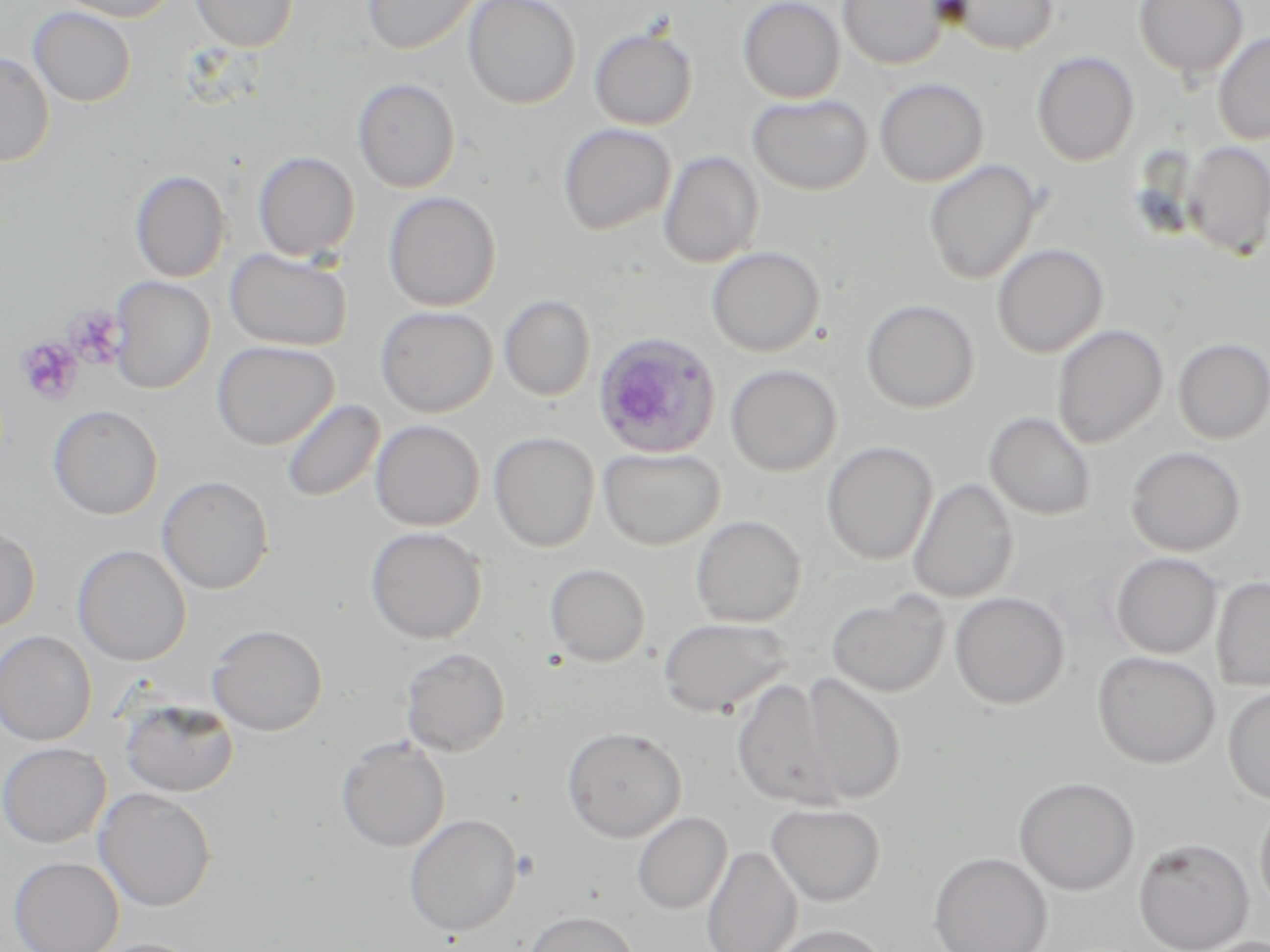

Approximate bounding boxes as [x1, y1, x2, y2] in pixels. Uninfected red blood cell locations: [52, 0, 182, 22], [190, 0, 298, 50], [362, 0, 483, 55], [463, 0, 581, 109], [737, 0, 846, 103], [837, 0, 950, 69], [944, 0, 1059, 56], [1133, 0, 1249, 80], [28, 6, 137, 107], [589, 26, 698, 130], [1213, 32, 1270, 145], [0, 51, 55, 167], [1032, 51, 1139, 166], [352, 78, 460, 193], [874, 78, 989, 187], [746, 93, 874, 196], [557, 123, 676, 235], [1183, 141, 1270, 258], [252, 150, 360, 262], [658, 151, 763, 268], [923, 159, 1044, 286], [130, 169, 230, 283], [382, 191, 502, 311], [992, 243, 1108, 358], [706, 246, 824, 357], [225, 247, 352, 351], [108, 275, 215, 394], [499, 294, 596, 401], [860, 299, 980, 413], [375, 305, 497, 417], [1051, 323, 1169, 448], [1172, 337, 1270, 444], [211, 340, 339, 450], [725, 364, 842, 477], [280, 398, 386, 503], [47, 403, 164, 520], [984, 411, 1096, 521], [370, 419, 485, 531], [489, 431, 599, 552], [821, 441, 938, 566], [597, 446, 725, 550], [1124, 446, 1246, 556], [157, 475, 274, 595], [907, 478, 1019, 604], [690, 514, 807, 627], [0, 526, 41, 632], [364, 526, 488, 644], [72, 544, 191, 666], [1110, 552, 1222, 659], [544, 563, 651, 667], [1211, 576, 1270, 691], [826, 591, 950, 697], [949, 591, 1070, 710], [658, 617, 793, 718], [207, 624, 327, 736], [0, 630, 97, 745], [399, 647, 511, 756], [1092, 651, 1221, 768], [797, 671, 906, 805], [730, 676, 844, 810], [1223, 685, 1270, 804], [119, 695, 239, 797], [562, 725, 686, 842], [335, 736, 451, 853], [0, 742, 110, 848], [1013, 776, 1140, 896], [93, 787, 217, 912], [1254, 797, 1270, 917], [766, 802, 887, 907], [631, 811, 732, 915], [404, 813, 522, 937], [1133, 837, 1255, 952], [700, 845, 802, 952], [927, 851, 1053, 952], [8, 855, 124, 952], [522, 910, 641, 952], [769, 923, 890, 952], [83, 938, 209, 952]. Plasmodium ovale-infected red blood cell locations: [591, 331, 723, 460]. Platelet locations: [65, 306, 125, 368], [17, 336, 84, 405]. Slide-level diagnosis: Plasmodium ovale. Single field of view. Light microscopy. Captured at 1000x magnification. Image is 1270×952 pixels. May-Grünwald-Giemsa stain. Thin blood film.